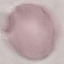

Summary:
  - Malaria status: uninfected
  - Capture: smartphone camera at the microscope eyepiece
  - Stain: Giemsa
  - Image type: cell patch, automatically extracted from a larger field of view and resized to 64 × 64 pixels
  - Preparation: thin blood film